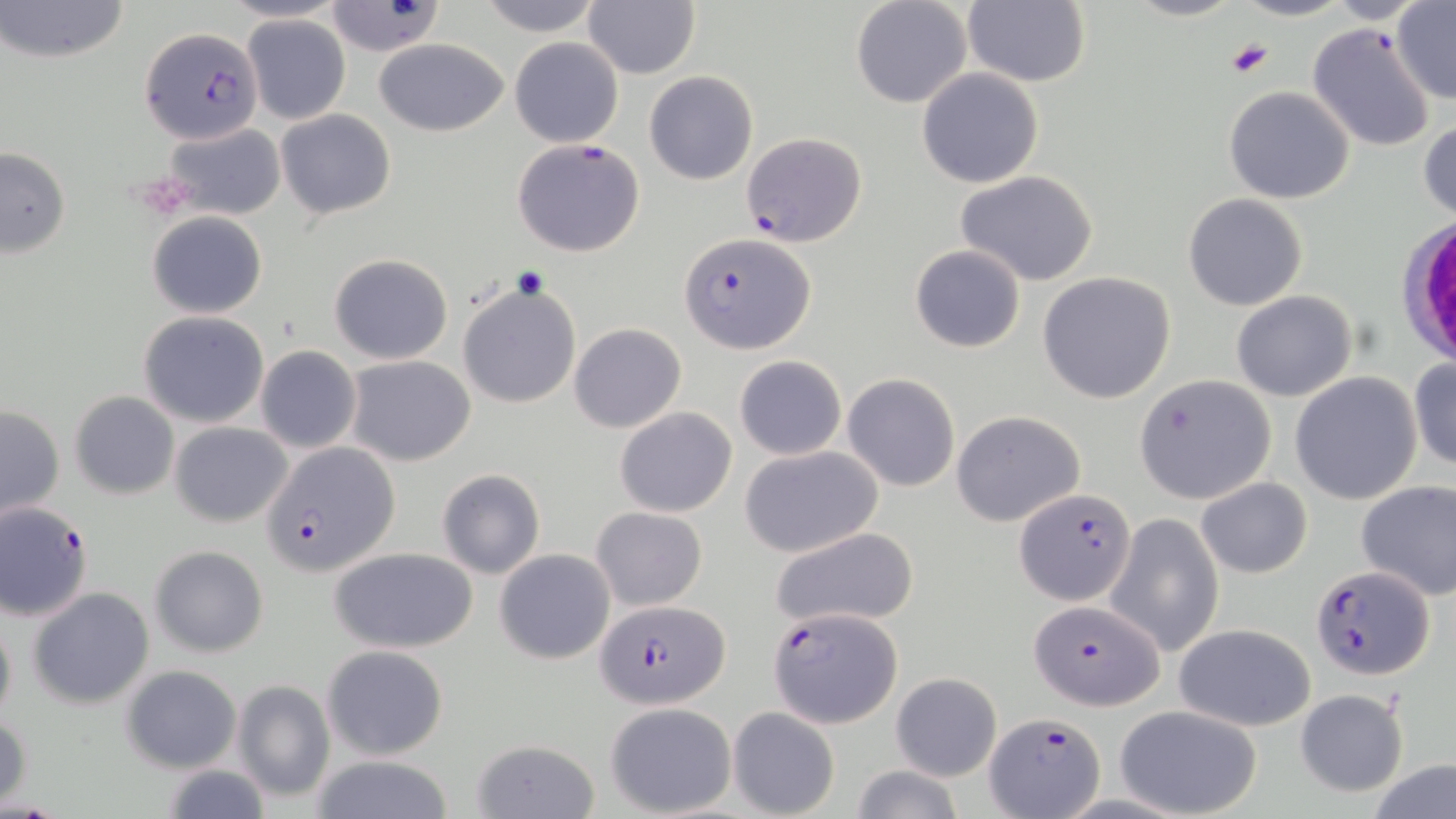 Approximate bounding boxes as (x1,y1)-(x2,y2) corner pairs in pixels. Plasmodium falciparum-infected red blood cell locations: (140,28)-(263,144), (741,132)-(866,247), (512,138)-(646,258), (679,232)-(814,354), (263,441)-(397,580), (1015,486)-(1135,605), (0,500)-(95,620), (1310,563)-(1432,679), (1030,599)-(1166,712), (596,600)-(728,710), (767,605)-(903,728), (985,712)-(1106,815). White blood cell locations: (1404,218)-(1455,363). Platelet locations: (1227,38)-(1274,79), (510,267)-(552,301). Uninfected red blood cell locations: (1,0)-(129,67), (476,0)-(605,34), (851,0)-(973,109), (964,0)-(1091,87), (1125,0)-(1243,22), (1230,0)-(1353,21), (583,2)-(700,79), (1390,2)-(1456,105), (325,3)-(444,57), (244,15)-(350,124), (1307,23)-(1437,152), (372,37)-(512,137), (509,37)-(624,148), (917,67)-(1045,188), (643,69)-(759,185), (1224,87)-(1354,204), (274,107)-(397,220), (1418,116)-(1456,225), (163,122)-(284,221), (0,146)-(72,259), (954,170)-(1102,287), (1184,193)-(1307,311), (147,211)-(268,319), (909,245)-(1026,353), (329,252)-(454,365), (1036,271)-(1175,403), (456,281)-(582,408), (1231,290)-(1357,402), (138,312)-(269,428), (568,322)-(687,433), (1261,327)-(1397,483), (255,345)-(362,453), (344,354)-(475,466), (733,355)-(847,460), (1409,358)-(1456,472), (843,372)-(961,491), (1289,372)-(1422,505), (1134,374)-(1275,504), (69,391)-(178,499), (1,403)-(65,523), (615,406)-(737,518), (951,409)-(1087,528), (170,421)-(293,526), (739,445)-(882,558), (436,469)-(545,578), (1196,476)-(1312,579), (1355,478)-(1455,600), (591,507)-(708,611), (1108,511)-(1223,656), (770,526)-(921,634), (149,544)-(270,659), (329,546)-(481,654), (494,549)-(615,664), (28,587)-(153,708), (0,610)-(16,730), (1173,622)-(1317,732), (321,644)-(449,760), (120,665)-(241,773), (891,672)-(1002,781), (232,680)-(335,803), (1295,688)-(1408,797), (605,702)-(738,817), (1114,704)-(1263,818), (729,708)-(839,817), (1,710)-(32,809), (470,738)-(599,818), (310,754)-(454,819), (1368,759)-(1456,818), (159,764)-(271,818), (850,765)-(964,819). Slide-level diagnosis: Plasmodium falciparum. 1000x magnification. Light microscopy. May-Grünwald-Giemsa-stained preparation. Single field of view. Image is 1456×819 pixels. Thin blood smear.